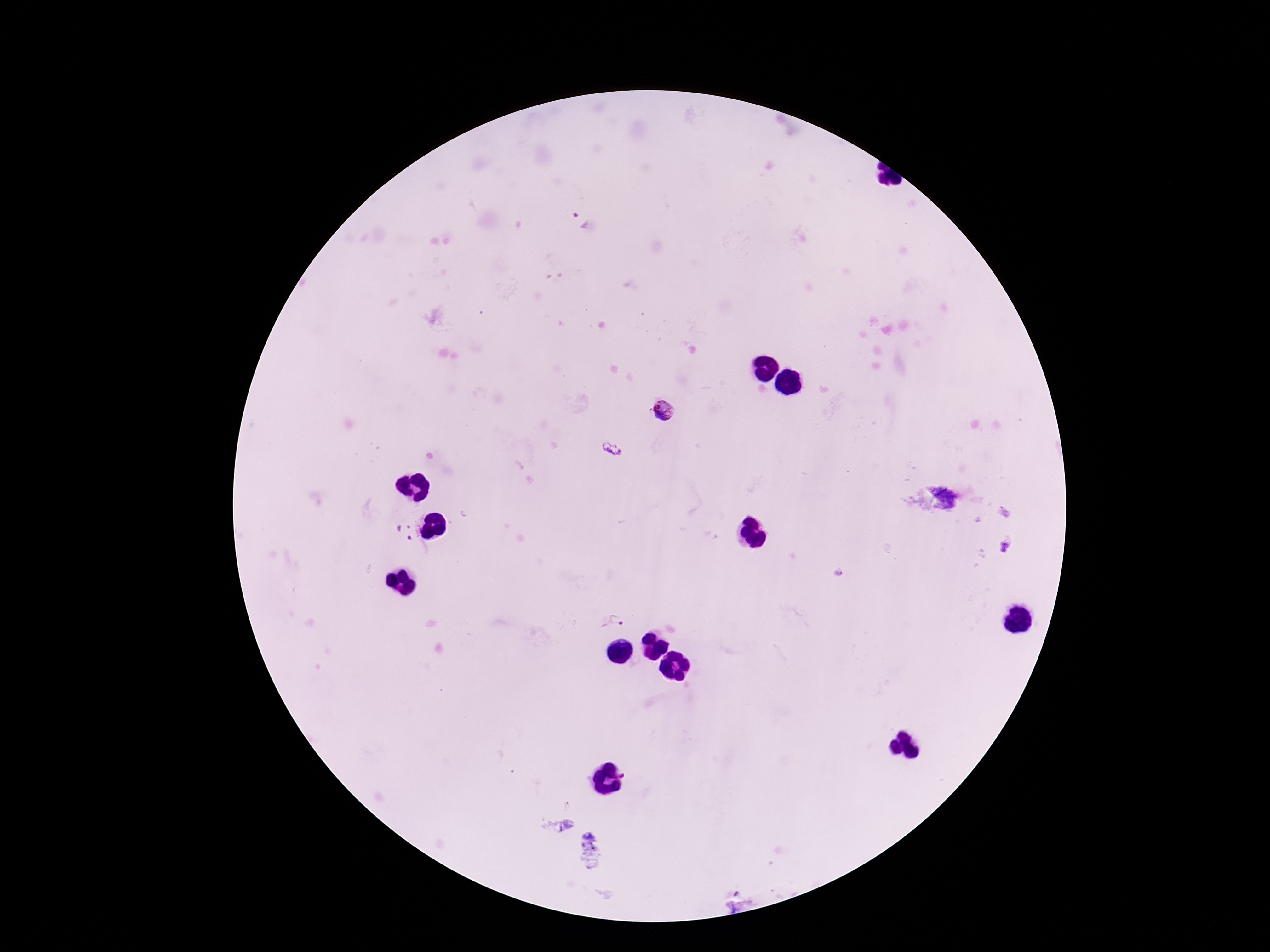 Approximate centers as {x, y} in pixels. Plasmodium parasite locations: {579, 218}, {664, 411}, {610, 449}, {403, 532}, {1007, 544}, {838, 572}, {613, 622}, {625, 774}. One field from this slide. Giemsa stain. 100x magnification. Image is 1270×952 pixels. Thick peripheral-blood smear. Patient malaria status: infected. Smartphone photograph taken through the microscope eyepiece.